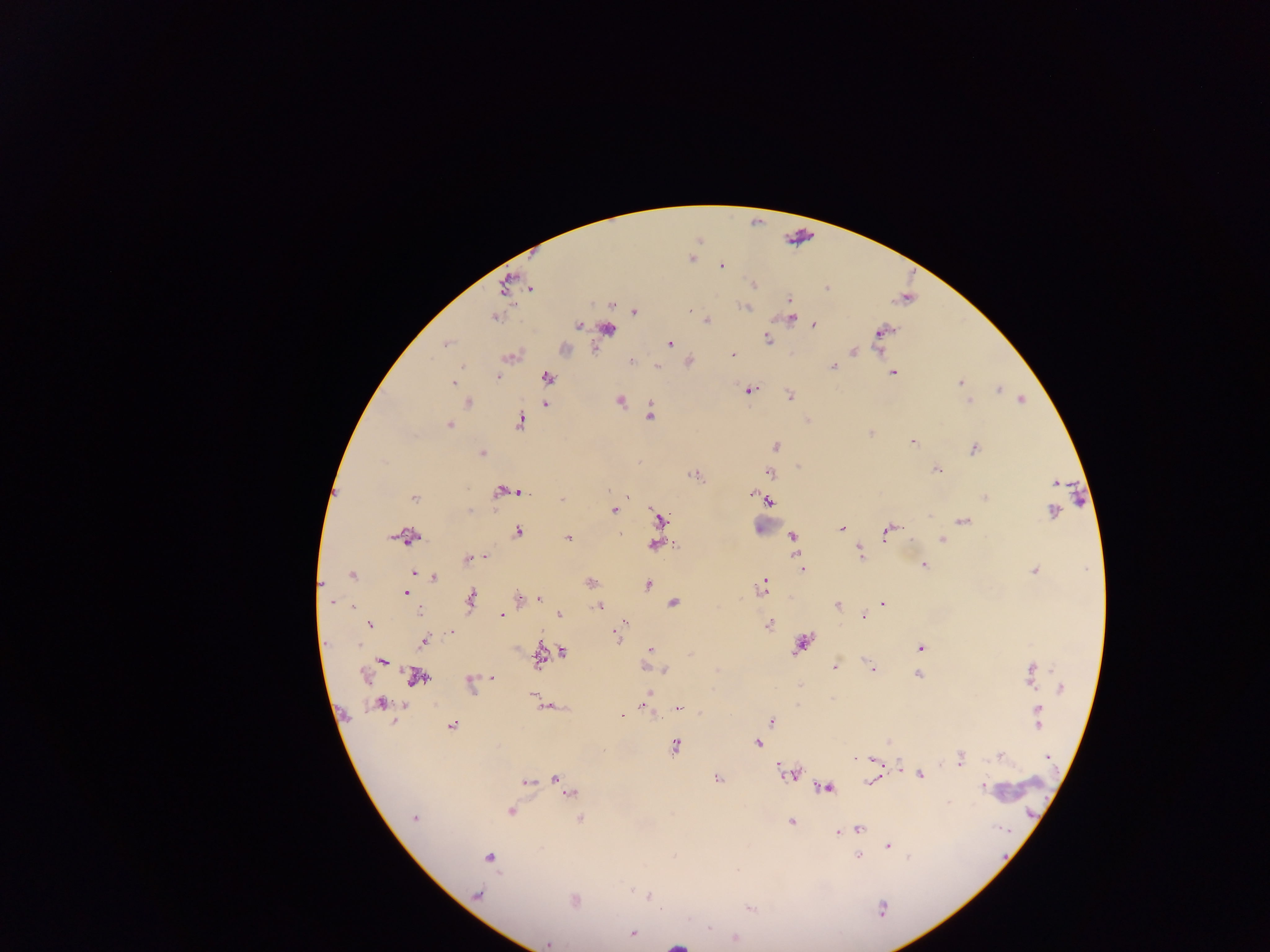
Approximate centers as [x, y] in pixels.
Summary:
  - Malaria parasite locations: [722, 267], [754, 284], [531, 288], [828, 288], [789, 299], [744, 307], [691, 310], [634, 311], [495, 318], [790, 318], [706, 320], [578, 325], [814, 325], [608, 328], [882, 332], [767, 339], [446, 343], [669, 343], [853, 351], [732, 355], [511, 356], [631, 361], [657, 366], [832, 366], [892, 372], [548, 377], [497, 378], [453, 382], [961, 382], [998, 389], [749, 390], [790, 396], [966, 397], [1022, 399], [620, 401], [969, 401], [468, 403], [546, 403], [650, 414], [519, 422], [448, 426], [870, 433], [912, 442], [775, 446], [974, 449], [482, 453], [936, 470], [770, 472], [695, 476], [609, 490], [515, 491], [503, 492], [752, 494], [414, 498], [628, 498], [985, 498], [562, 499], [768, 501], [469, 510], [613, 510], [1052, 511], [929, 516], [660, 518], [963, 521], [842, 528], [886, 531], [517, 532], [621, 534], [792, 536], [407, 537], [568, 539], [910, 540], [941, 540], [655, 545], [860, 554], [486, 557], [468, 558], [799, 561], [924, 565], [802, 569], [1034, 571], [415, 573], [352, 575], [435, 577], [590, 582], [764, 582], [647, 585], [762, 588], [406, 594], [519, 598], [470, 599], [538, 599], [330, 601], [673, 603], [883, 604], [837, 605], [352, 606], [598, 606], [420, 612], [558, 614], [501, 616], [864, 616], [624, 624], [768, 624], [370, 625], [451, 633], [617, 635], [424, 641], [357, 645], [801, 645], [920, 648], [649, 649], [563, 653], [538, 657], [382, 660], [870, 666], [645, 667], [835, 667], [873, 670], [664, 671], [1031, 674], [364, 675], [918, 675], [416, 676], [492, 677], [470, 684], [1061, 688], [649, 691], [532, 695], [379, 703], [644, 704], [797, 705], [547, 707], [678, 708], [1037, 709], [622, 715], [1038, 718], [772, 721], [451, 726], [888, 742], [758, 743], [675, 747], [1001, 755], [1048, 757], [960, 758], [855, 759], [874, 760], [899, 766], [789, 774], [920, 774], [556, 779], [717, 779], [525, 782], [870, 782], [564, 788], [826, 788], [982, 788], [570, 792], [948, 802], [510, 811], [414, 818], [580, 819], [791, 822], [859, 829], [851, 830], [838, 833], [888, 846], [859, 856], [490, 857], [477, 895], [649, 896], [575, 900], [750, 909], [882, 909], [633, 934], [734, 937], [548, 944]
  - Object labeled both malaria parasite and leukocyte by the source: [678, 945]
  - Leukocyte locations: [762, 525], [1018, 787]
  - Preparation: thick blood film
  - Image size: 1270×952 pixels
  - Capture: mobile-phone photograph through a microscope
  - Field of view: single
  - Country: Ghana